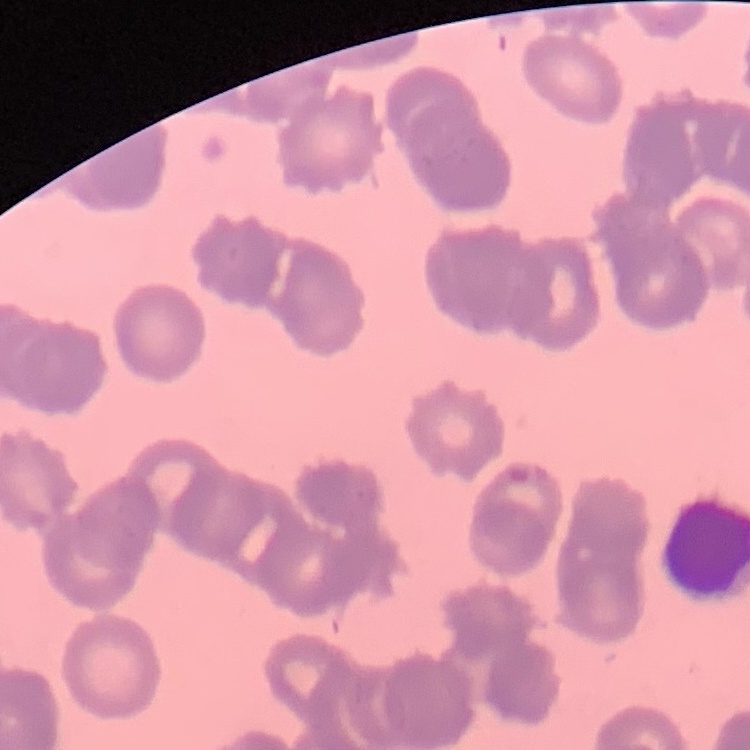

erythrocyte_morphology: rouleaux formation
image_type: one tile cut from a larger photomicrograph
preparation: thin peripheral smear
stain: Field's or Giemsa